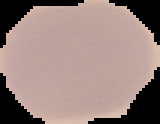
image type = segmented cell region on a black background
image size = 160×124 pixels
preparation = thin blood smear
result = negative for malaria parasites